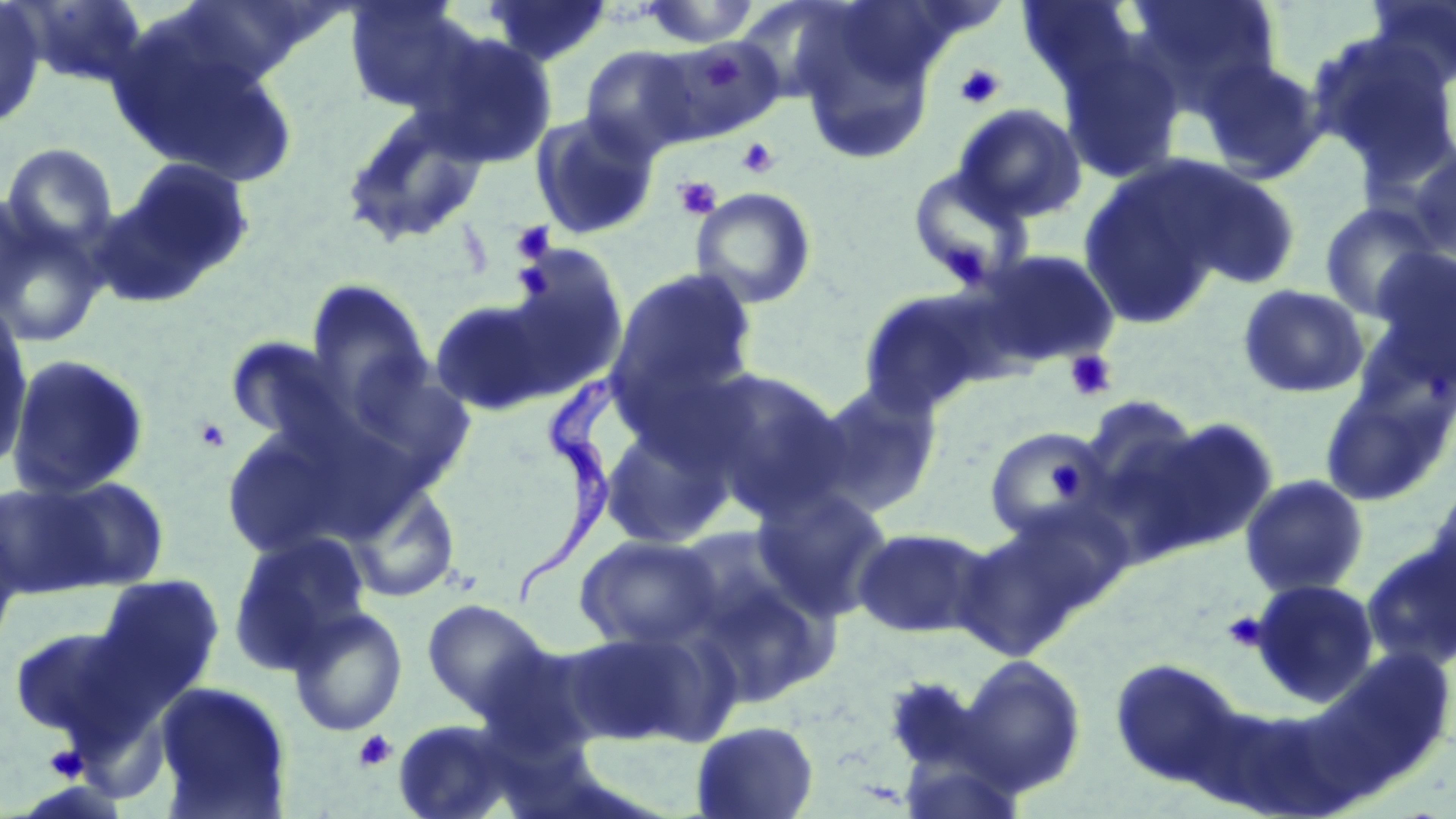
Summary:
  - Coordinate format: approximate bounding boxes as [x1, y1, x2, y2] in pixels
  - Trypanosoma brucei locations: [512, 370, 632, 611]
  - Uninfected red blood cell locations: [15, 0, 150, 89], [342, 0, 479, 115], [481, 0, 613, 68], [1017, 0, 1144, 95], [1127, 0, 1282, 112], [1363, 0, 1456, 91], [0, 1, 47, 130], [636, 1, 761, 48], [109, 21, 299, 187], [797, 23, 936, 166], [415, 31, 558, 168], [1310, 33, 1456, 179], [1059, 43, 1186, 185], [579, 45, 703, 160], [1197, 57, 1328, 183], [952, 103, 1087, 223], [340, 105, 492, 249], [529, 110, 660, 241], [1, 142, 120, 255], [1405, 148, 1456, 266], [115, 156, 257, 290], [1173, 163, 1303, 290], [906, 164, 1035, 291], [1078, 164, 1231, 329], [690, 186, 818, 309], [0, 190, 37, 320], [1318, 201, 1440, 321], [0, 208, 108, 350], [490, 243, 631, 397], [1368, 246, 1456, 380], [970, 248, 1120, 369], [605, 266, 760, 419], [304, 280, 435, 421], [1237, 283, 1370, 399], [856, 287, 996, 417], [427, 295, 564, 417], [0, 302, 35, 478], [224, 335, 359, 451], [332, 351, 477, 498], [5, 353, 150, 501], [692, 368, 850, 521], [803, 378, 945, 521], [1318, 379, 1453, 508], [1077, 394, 1206, 519], [594, 412, 738, 550], [1140, 414, 1280, 552], [219, 418, 380, 562], [982, 425, 1111, 543], [1238, 474, 1371, 598], [37, 476, 172, 591], [1422, 479, 1456, 618], [0, 480, 117, 599], [347, 480, 461, 603], [752, 486, 895, 621], [0, 511, 26, 658], [952, 511, 1110, 662], [852, 526, 992, 638], [226, 532, 372, 673], [574, 534, 724, 652], [1362, 540, 1456, 671], [686, 550, 839, 708], [93, 574, 225, 701], [1249, 578, 1380, 705], [421, 598, 551, 718], [286, 604, 408, 737], [9, 624, 140, 742], [565, 625, 722, 746], [958, 654, 1087, 796], [1109, 657, 1248, 793], [154, 681, 293, 818], [390, 718, 525, 819], [690, 719, 820, 819]
  - Platelet locations: [703, 52, 744, 87], [954, 63, 1006, 109], [736, 137, 780, 179], [674, 176, 722, 220], [510, 222, 556, 263], [946, 245, 991, 291], [1065, 350, 1117, 401], [193, 417, 232, 454], [1049, 457, 1083, 501], [1223, 610, 1269, 651], [353, 729, 397, 772], [44, 744, 87, 781]
  - Slide-level diagnosis: Trypanosoma brucei
  - Image size: 1456×819 pixels
  - Stain: May-Grünwald-Giemsa
  - Preparation: thin blood smear
  - Field of view: single
  - Modality: light microscopy
  - Magnification: 1000x